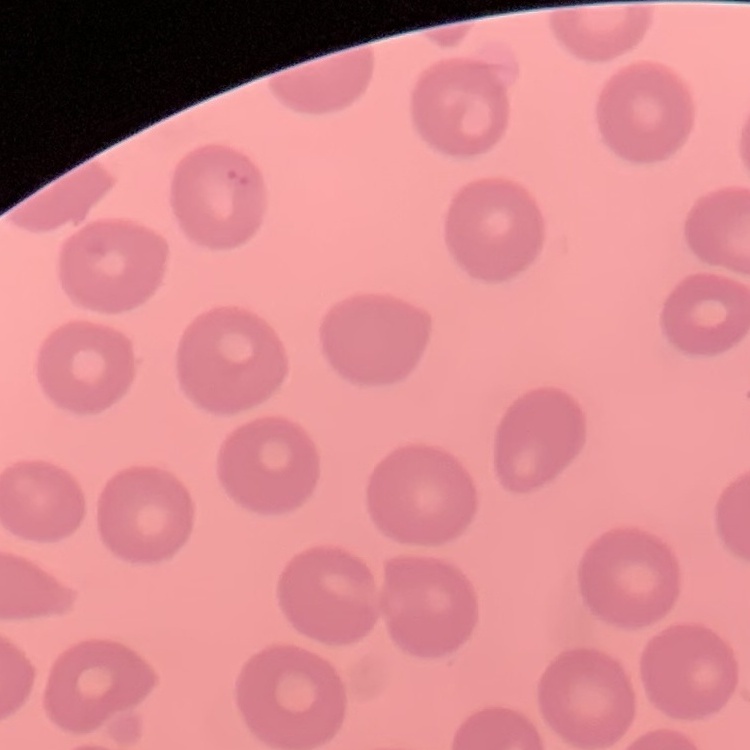 The erythrocytes show no rouleaux formation. Stained with either Field's or Giemsa. Square crop of a larger photomicrograph. Thin blood film.